State which parasite is depicted.
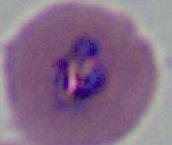
This is Plasmodium.

400x or 1000x magnification. Micrograph.